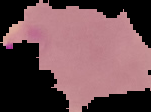

Summary:
  - Image type: segmented cell region on a black background
  - Image size: 151×112 pixels
  - Preparation: thin blood smear
  - Malaria status: parasitized